Classify this cell by malaria status.
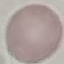
Uninfected.

capture = smartphone camera at the microscope eyepiece
stain = Giemsa
preparation = thin blood smear
image type = automatically extracted cell patch, resized to 64 × 64 pixels